Name the cell type shown.
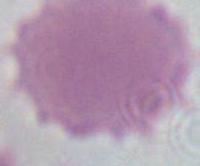

This is an erythrocyte.

Summary:
  - Modality: photomicrograph
  - Magnification: 1000x